Report the malaria status of this cell.
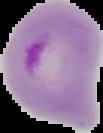

It is parasitized.

image size = 103×133 pixels
preparation = thin blood film
image type = segmented cell region on a black background